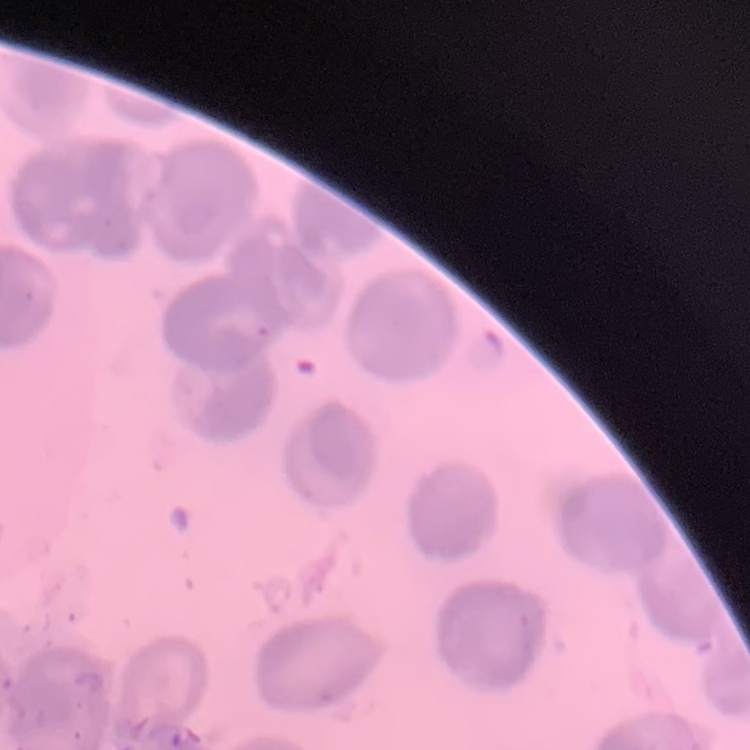

The red blood cells exhibit no rouleaux formation. Stained with either Field's or Giemsa. Thin blood smear. Square crop of a larger photomicrograph.